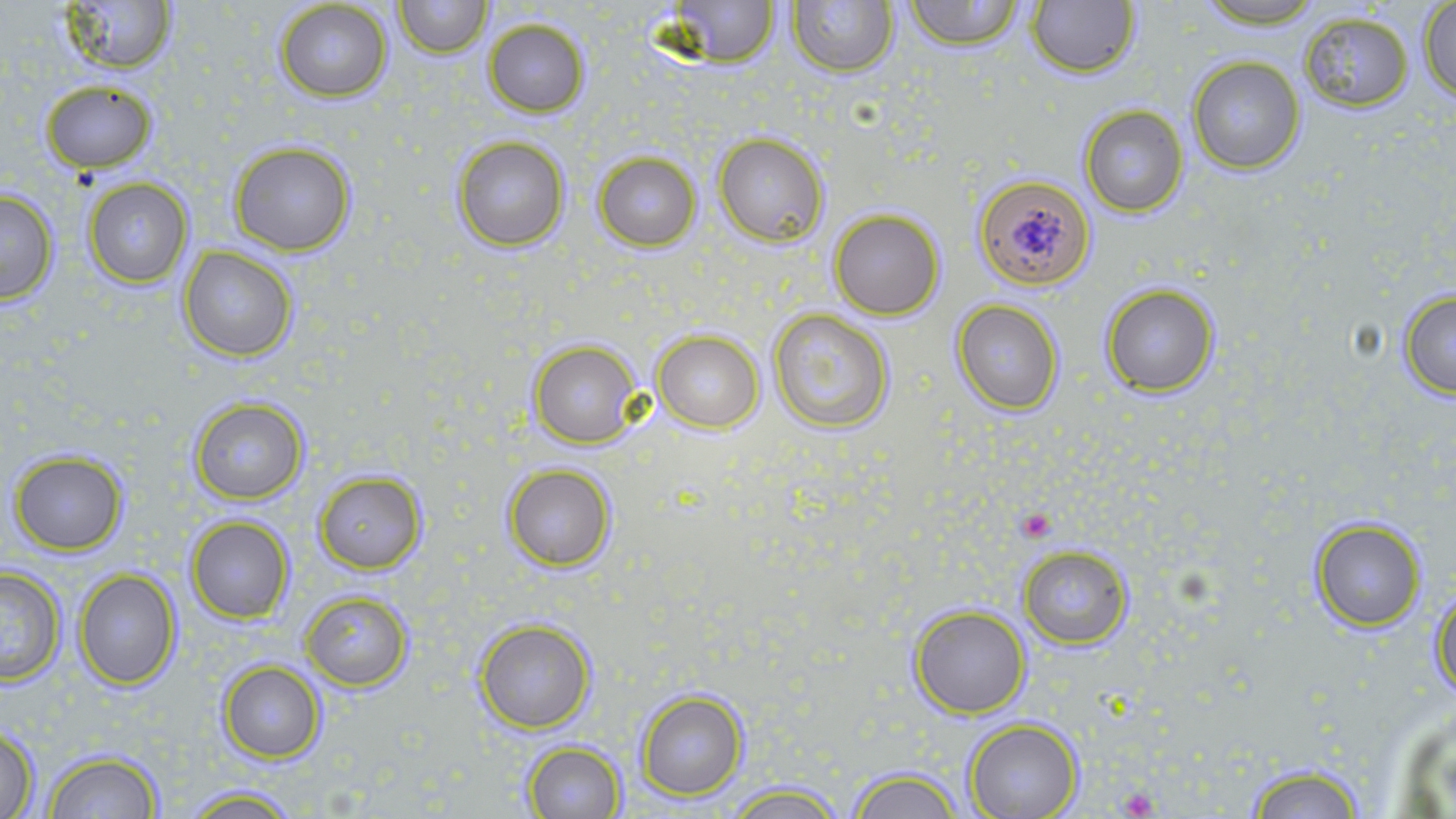
slide-level diagnosis = Plasmodium falciparum
modality = optical microscopy
field of view = single
image size = 1456×819 pixels
uninfected red blood cell locations = approximate bounding boxes as (x1, y1, x2, y2) in pixels: (59, 0, 175, 75), (392, 0, 489, 57), (663, 0, 781, 67), (902, 0, 1025, 50), (1025, 0, 1139, 79), (1190, 0, 1333, 28), (273, 1, 395, 104), (788, 2, 897, 78), (1419, 3, 1455, 102), (1297, 10, 1415, 112), (481, 17, 592, 116), (1187, 57, 1306, 173), (39, 78, 157, 173), (1078, 105, 1189, 217), (713, 133, 830, 247), (450, 135, 571, 251), (231, 141, 356, 256), (592, 151, 701, 252), (974, 173, 1096, 290), (82, 177, 193, 287), (0, 188, 59, 305), (828, 208, 945, 319), (179, 246, 299, 362), (1100, 282, 1221, 399), (1396, 287, 1456, 399), (951, 299, 1065, 417), (767, 308, 895, 433), (653, 329, 765, 434), (528, 340, 643, 448), (189, 396, 310, 505), (8, 451, 128, 554), (503, 465, 616, 569), (314, 470, 427, 572), (186, 515, 295, 624), (1311, 517, 1427, 632), (1018, 544, 1132, 649), (0, 566, 65, 686), (74, 568, 181, 689), (1430, 584, 1456, 701), (300, 590, 412, 691), (909, 605, 1031, 718), (474, 618, 597, 734), (217, 660, 326, 763), (635, 688, 749, 803), (1387, 705, 1456, 813), (963, 718, 1083, 819), (1, 727, 41, 817), (521, 742, 629, 819), (45, 749, 164, 818), (1243, 762, 1371, 818), (847, 766, 967, 819), (719, 781, 850, 818), (175, 786, 309, 818)
stain = May-Grünwald-Giemsa
preparation = thin blood smear
platelet locations = approximate bounding boxes as (x1, y1, x2, y2) in pixels: (1015, 506, 1059, 542)
magnification = 1000x